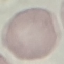

malaria status = uninfected
image type = cell patch, automatically extracted from a larger field of view and resized to 64 × 64 pixels
stain = Giemsa
capture = smartphone through the microscope eyepiece
preparation = thin smear